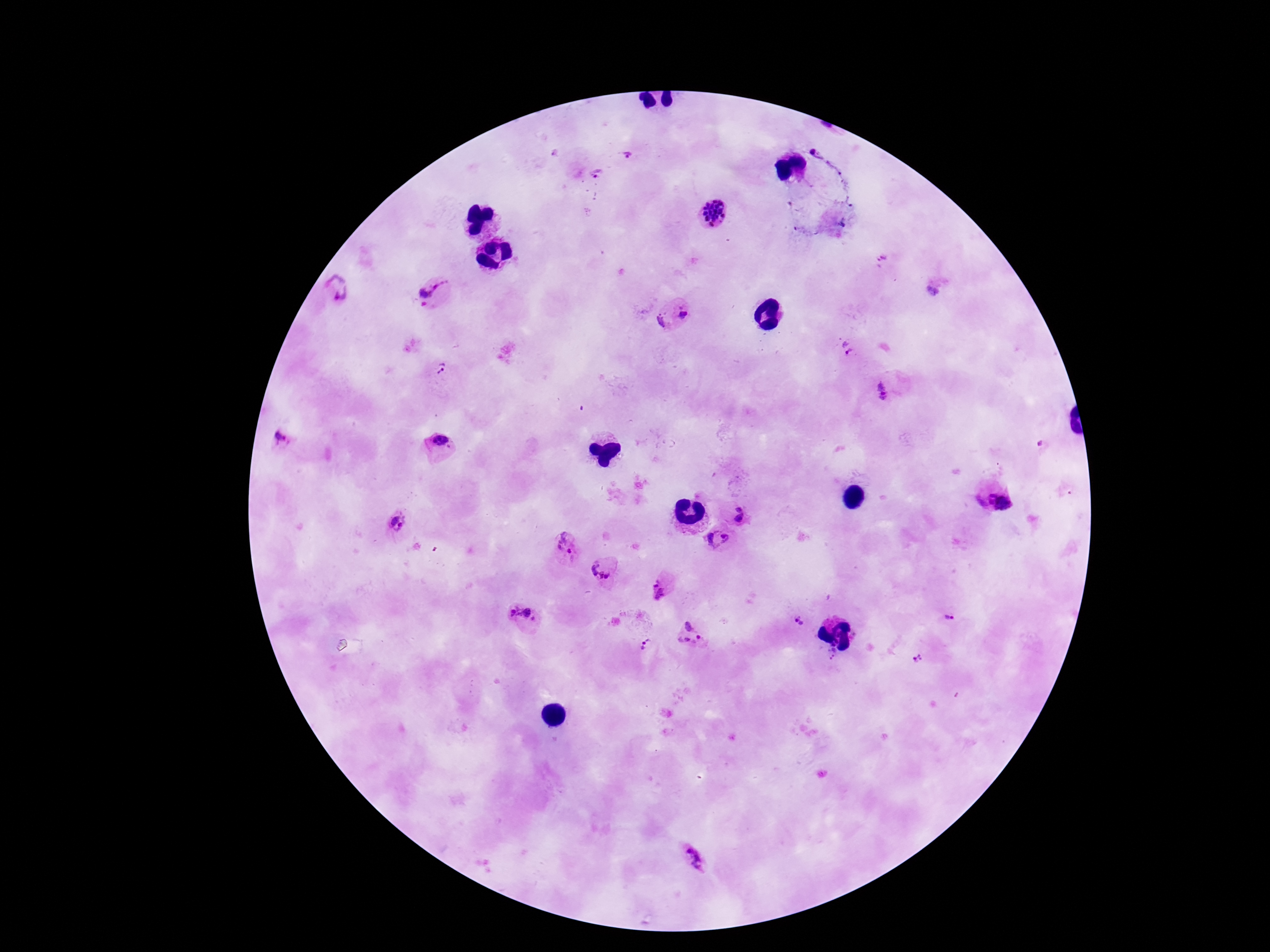

capture = smartphone camera through the microscope eyepiece
stain = Giemsa
Plasmodium parasite locations = approximate centers as [x, y] in pixels: [626, 156], [597, 173], [715, 212], [336, 292], [434, 293], [683, 313], [661, 321], [846, 346], [440, 368], [884, 392], [282, 439], [438, 439], [999, 502], [737, 513], [398, 521], [718, 536], [563, 543], [603, 567], [662, 592], [520, 615], [950, 618], [800, 621], [689, 635], [647, 645], [831, 651], [919, 659], [696, 858]
field of view = single
patient malaria status = infected
magnification = 100x
image size = 1270×952 pixels
preparation = thick peripheral-blood smear